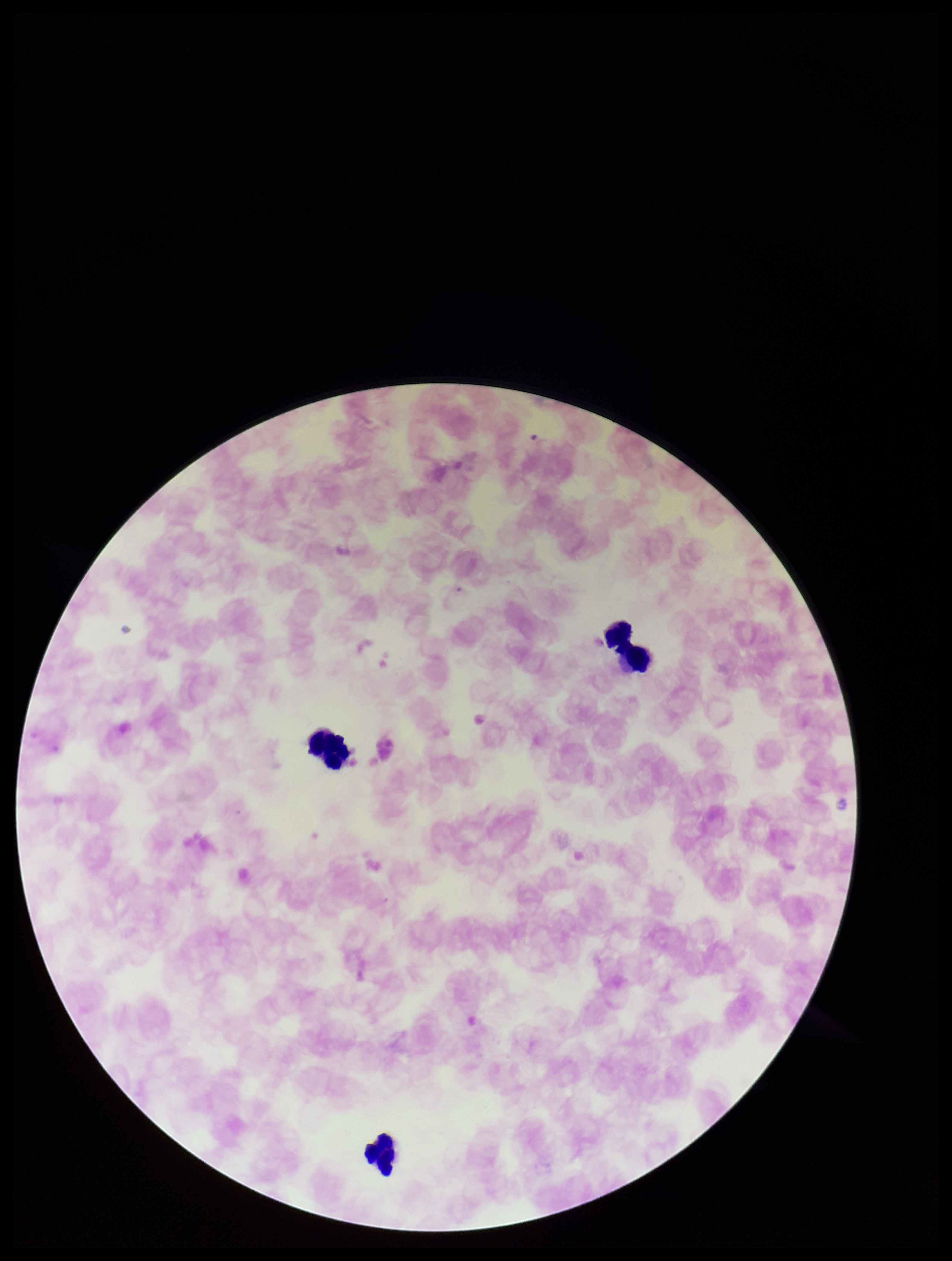 Plasmodium parasites: none seen. One field from this slide. Parasite count: 0. Preparation: thick. Species reported for this patient: Plasmodium falciparum. Smartphone photograph taken through the eyepiece of a microscope. Leukocyte count: 4. Stained with Giemsa. Image is 952×1261 pixels. Patient malaria status: infected.